Identify the parasite.
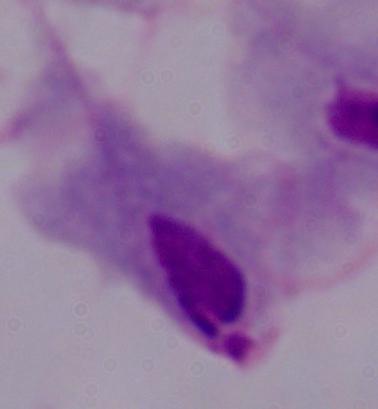

This is a trichomonad.

Micrograph. 1000x magnification.